Identify the parasite.
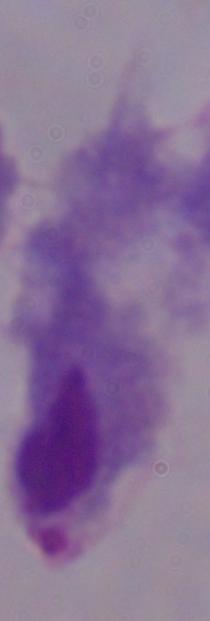
This is a trichomonad.

Micrograph. Captured at 1000x magnification.